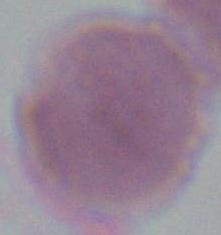

modality = micrograph
identification = red blood cell
magnification = 1000x